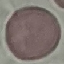

malaria_status: uninfected
preparation: thin blood film
image_type: automatically extracted cell patch, resized to 64 × 64 pixels
capture: smartphone through the microscope eyepiece
stain: Giemsa